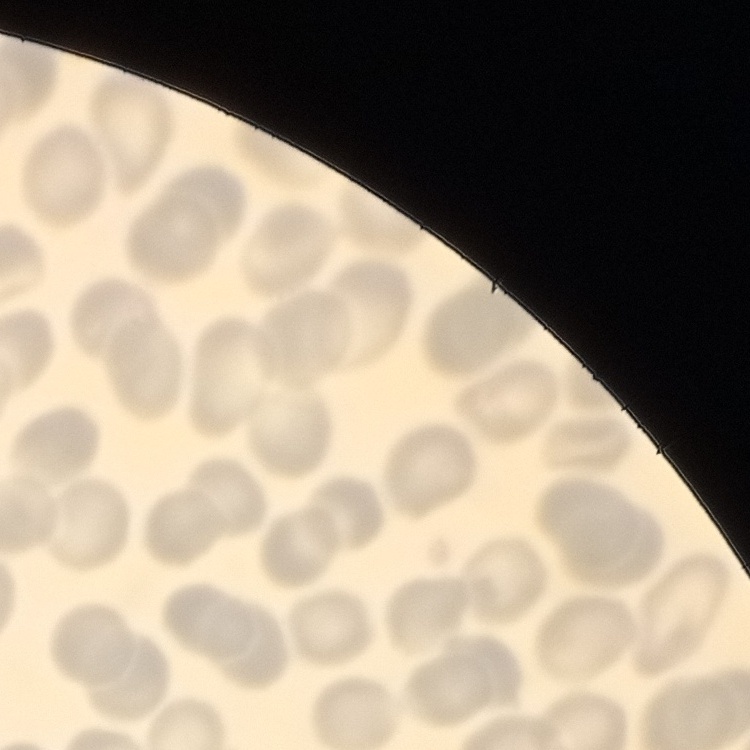

Summary:
  - Erythrocyte morphology: no rouleaux formation
  - Stain: Field's or Giemsa
  - Image type: one tile cut from a larger photomicrograph
  - Preparation: thin peripheral smear